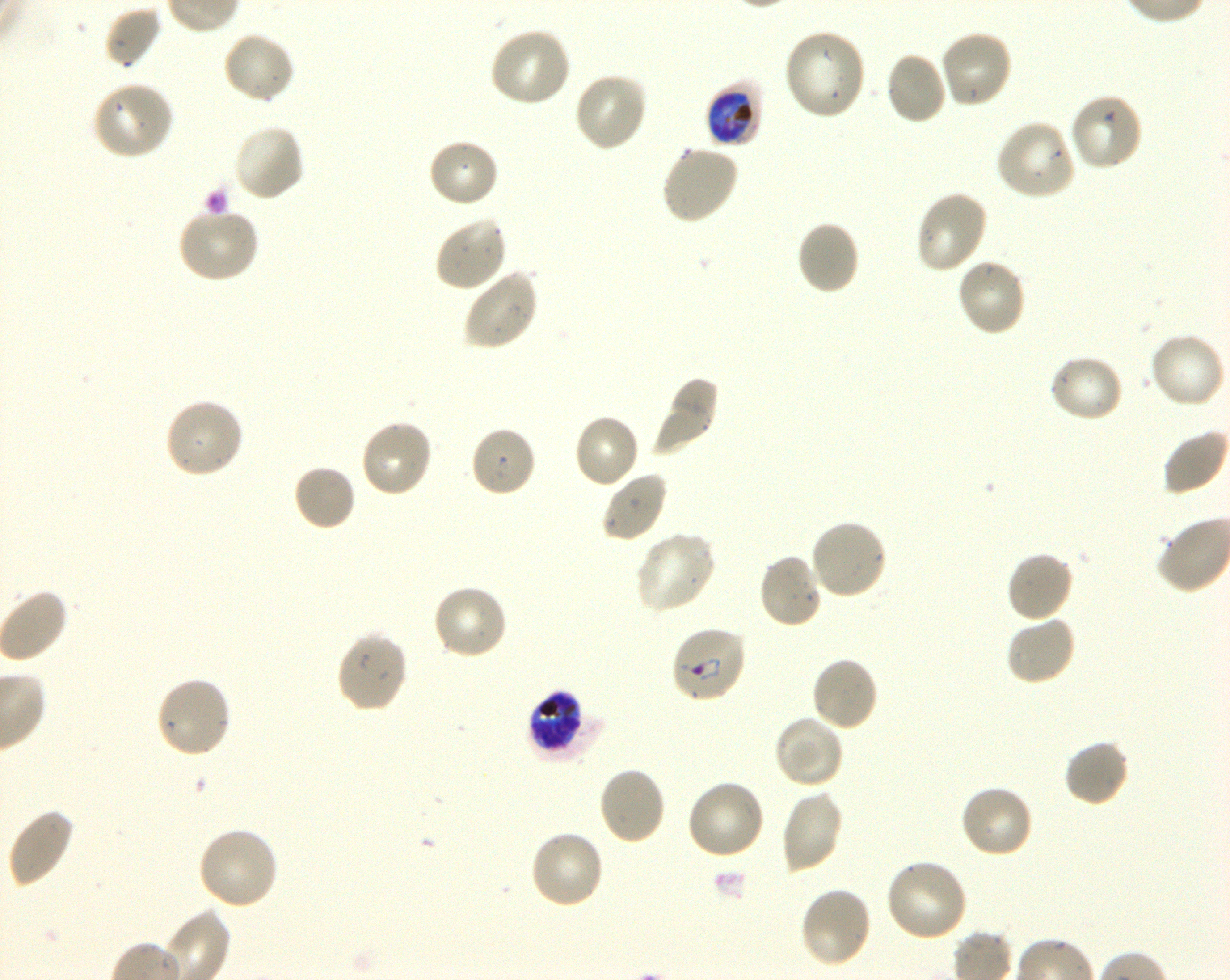
Approximate bounding boxes as (x1, y1, x2, y2) in pixels. Not every red blood cell is marked. A life-cycle stage — or a range of stages, where the recorded stages span more than one — follows each staged infected red blood cell.
Summary:
  - Locations of uninfected red blood cells: (105, 6, 163, 69), (488, 26, 573, 109), (782, 27, 868, 122), (938, 29, 1013, 110), (222, 31, 297, 105), (885, 51, 949, 126), (573, 71, 649, 153), (91, 80, 174, 161), (1067, 93, 1144, 173), (994, 119, 1076, 202), (232, 123, 307, 202), (428, 137, 501, 208), (660, 144, 740, 225), (913, 189, 989, 275), (176, 207, 261, 285), (433, 214, 509, 293), (796, 220, 861, 296), (956, 258, 1028, 338), (463, 267, 540, 351), (1149, 331, 1227, 410), (1048, 353, 1125, 423), (648, 376, 720, 457), (164, 396, 245, 480), (572, 413, 640, 490), (359, 418, 434, 498), (469, 426, 537, 498), (292, 463, 357, 532), (601, 470, 668, 543), (808, 518, 888, 601), (634, 530, 717, 614), (1005, 550, 1074, 623), (757, 553, 824, 630), (431, 584, 509, 662), (1004, 615, 1078, 687), (335, 629, 409, 714), (809, 655, 880, 731), (153, 675, 232, 760), (773, 714, 845, 789), (1063, 739, 1130, 807), (598, 766, 667, 846), (685, 777, 767, 861), (958, 782, 1035, 859), (779, 790, 844, 874), (6, 807, 76, 889), (197, 826, 280, 910), (527, 828, 605, 910), (883, 858, 969, 943), (798, 886, 873, 969)
  - Locations of infected red blood cells: (705, 80, 763, 147) late trophozoite to early schizont; (670, 625, 748, 704) ring; (527, 689, 599, 761) late trophozoite to late schizont
  - Culture: shaking in-vitro P. falciparum strain 3D7
  - Donor blood group: O+
  - Objective: 100x, oil immersion, numerical aperture 1.30
  - Field of view: one from this slide
  - Preparation: thin blood smear
  - Image size: 1230×980 pixels
  - Stain: Giemsa